Mark where platelets are.
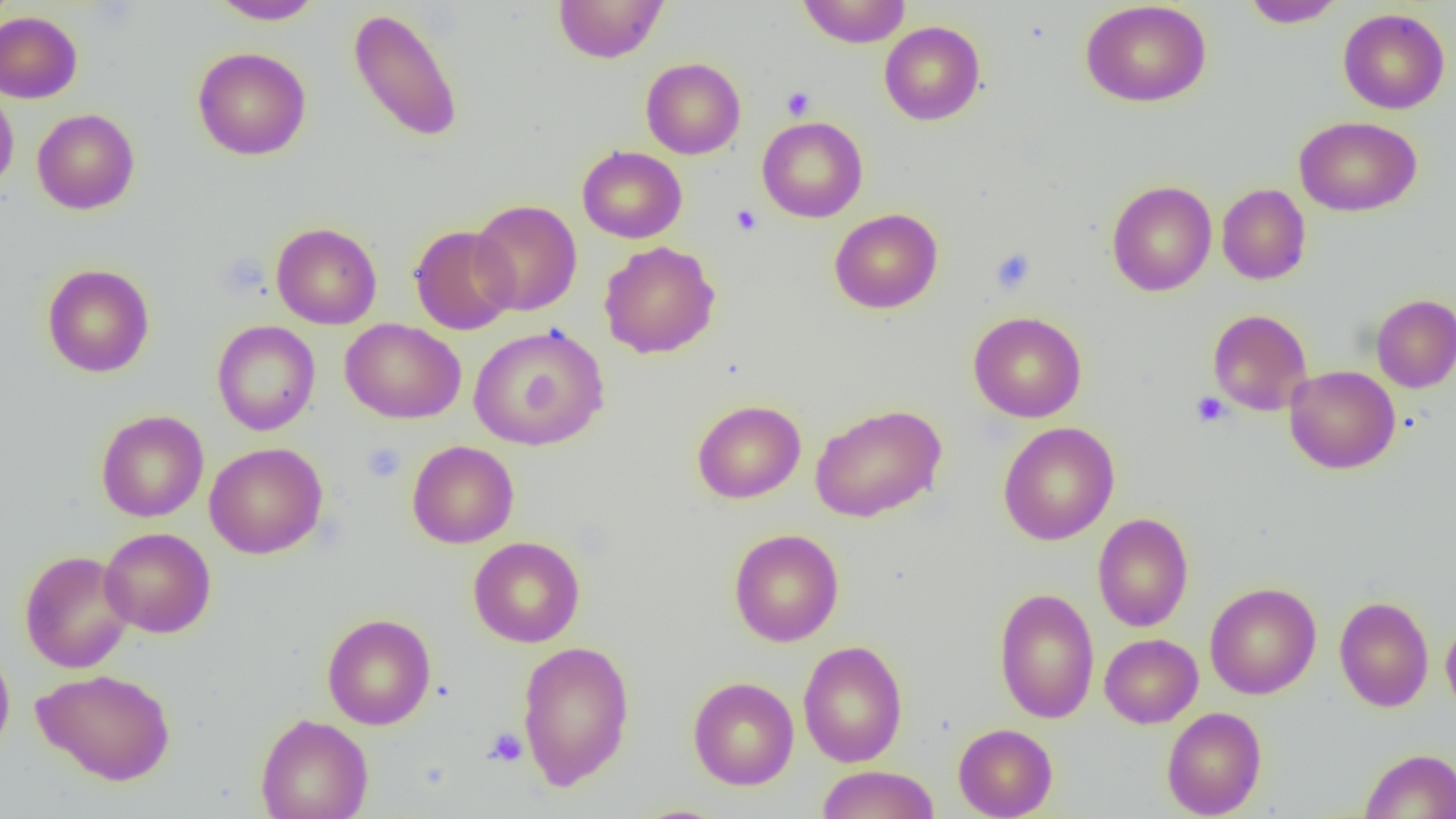

Approximate bounding boxes as (x1, y1, x2, y2) in pixels.
Platelets: (781, 87, 815, 120), (731, 204, 762, 235), (990, 248, 1036, 294), (1191, 392, 1230, 427), (361, 442, 406, 483), (484, 727, 528, 767).

slide-level diagnosis = negative for blood parasites
magnification = 1000x
field of view = one of a larger specimen
image size = 1456×819 pixels
modality = light microscopy
uninfected red blood cell locations = approximate bounding boxes as (x1, y1, x2, y2) in pixels: (553, 0, 669, 63), (798, 0, 911, 47), (1241, 0, 1344, 28), (207, 1, 325, 24), (1080, 1, 1212, 107), (349, 8, 464, 143), (1338, 8, 1450, 114), (0, 11, 82, 103), (879, 21, 985, 125), (193, 47, 311, 160), (641, 57, 745, 159), (0, 87, 19, 196), (32, 108, 140, 214), (757, 116, 868, 222), (1294, 116, 1421, 216), (577, 146, 687, 243), (1106, 180, 1216, 296), (1217, 183, 1311, 285), (470, 199, 582, 316), (830, 208, 943, 313), (271, 222, 382, 329), (409, 225, 519, 335), (599, 241, 720, 359), (42, 264, 155, 377), (1371, 294, 1456, 393), (1207, 309, 1313, 415), (968, 311, 1087, 423), (340, 319, 466, 424), (212, 320, 320, 436), (337, 323, 607, 426), (468, 324, 610, 451), (1284, 365, 1401, 474), (692, 399, 806, 503), (810, 403, 947, 523), (96, 410, 209, 522), (998, 422, 1119, 545), (407, 440, 519, 548), (204, 442, 328, 559), (1093, 513, 1193, 632), (100, 527, 216, 638), (729, 528, 844, 647), (469, 536, 585, 647), (19, 550, 135, 673), (1205, 582, 1321, 700), (993, 587, 1100, 723), (1334, 596, 1433, 711), (322, 613, 436, 729), (1441, 617, 1456, 719), (1100, 633, 1203, 728), (517, 640, 635, 790), (797, 640, 908, 767), (0, 644, 15, 760), (32, 668, 176, 785), (688, 676, 799, 790), (1162, 706, 1267, 818), (255, 713, 374, 819), (953, 723, 1057, 818), (1360, 748, 1456, 818), (815, 765, 940, 819)
preparation = thin blood film